Give the extent of all Plasmodium vivax-infected red blood cells.
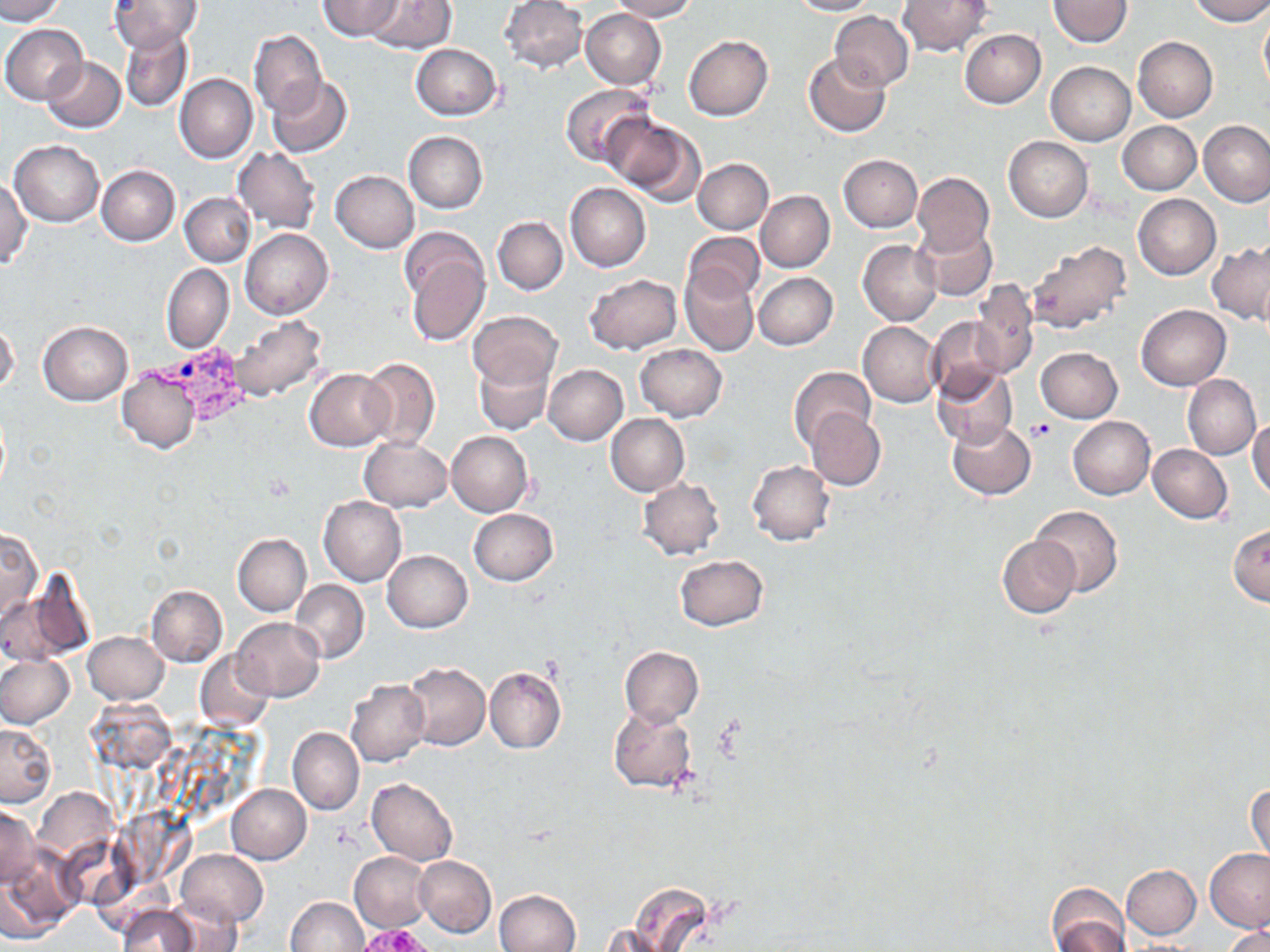

Approximate bounding boxes as named x1/y1/x2/y2 corners in pixels.
Plasmodium vivax-infected red blood cells: (x1=140, y1=342, x2=257, y2=429).

Uninfected red blood cell locations: (x1=0, y1=0, x2=64, y2=24), (x1=318, y1=0, x2=402, y2=40), (x1=363, y1=0, x2=454, y2=53), (x1=500, y1=0, x2=587, y2=73), (x1=610, y1=0, x2=696, y2=21), (x1=787, y1=0, x2=877, y2=17), (x1=899, y1=0, x2=993, y2=57), (x1=1048, y1=0, x2=1133, y2=48), (x1=1188, y1=0, x2=1270, y2=25), (x1=107, y1=1, x2=203, y2=53), (x1=1258, y1=7, x2=1270, y2=96), (x1=580, y1=8, x2=666, y2=90), (x1=830, y1=11, x2=913, y2=90), (x1=1, y1=24, x2=87, y2=105), (x1=120, y1=26, x2=194, y2=112), (x1=248, y1=29, x2=327, y2=118), (x1=960, y1=29, x2=1046, y2=107), (x1=684, y1=34, x2=773, y2=120), (x1=1133, y1=37, x2=1218, y2=121), (x1=411, y1=44, x2=502, y2=121), (x1=803, y1=52, x2=890, y2=137), (x1=42, y1=57, x2=126, y2=132), (x1=1046, y1=61, x2=1135, y2=145), (x1=174, y1=74, x2=257, y2=163), (x1=268, y1=76, x2=353, y2=158), (x1=559, y1=83, x2=653, y2=170), (x1=603, y1=113, x2=703, y2=204), (x1=1198, y1=120, x2=1270, y2=208), (x1=1119, y1=121, x2=1200, y2=194), (x1=404, y1=131, x2=487, y2=213), (x1=1004, y1=136, x2=1093, y2=222), (x1=10, y1=140, x2=104, y2=226), (x1=233, y1=147, x2=322, y2=233), (x1=838, y1=154, x2=923, y2=231), (x1=693, y1=159, x2=773, y2=234), (x1=97, y1=164, x2=180, y2=246), (x1=331, y1=170, x2=419, y2=252), (x1=913, y1=172, x2=994, y2=255), (x1=0, y1=176, x2=31, y2=269), (x1=565, y1=182, x2=651, y2=272), (x1=755, y1=190, x2=834, y2=272), (x1=181, y1=193, x2=254, y2=267), (x1=1133, y1=194, x2=1220, y2=279), (x1=493, y1=217, x2=568, y2=295), (x1=913, y1=223, x2=996, y2=301), (x1=241, y1=229, x2=333, y2=319), (x1=399, y1=232, x2=489, y2=346), (x1=683, y1=232, x2=765, y2=304), (x1=859, y1=240, x2=942, y2=325), (x1=1026, y1=241, x2=1132, y2=335), (x1=1207, y1=242, x2=1270, y2=324), (x1=161, y1=264, x2=234, y2=353), (x1=680, y1=267, x2=758, y2=356), (x1=755, y1=273, x2=838, y2=350), (x1=584, y1=274, x2=681, y2=355), (x1=969, y1=281, x2=1038, y2=379), (x1=1136, y1=305, x2=1231, y2=389), (x1=469, y1=311, x2=561, y2=389), (x1=927, y1=315, x2=1006, y2=400), (x1=228, y1=316, x2=329, y2=401), (x1=37, y1=321, x2=132, y2=405), (x1=858, y1=321, x2=941, y2=407), (x1=0, y1=322, x2=20, y2=395), (x1=635, y1=342, x2=727, y2=421), (x1=1036, y1=347, x2=1123, y2=423), (x1=473, y1=354, x2=553, y2=436), (x1=359, y1=357, x2=440, y2=451), (x1=542, y1=365, x2=628, y2=445), (x1=932, y1=365, x2=1018, y2=448), (x1=117, y1=366, x2=201, y2=453), (x1=305, y1=368, x2=394, y2=451), (x1=789, y1=368, x2=875, y2=452), (x1=1182, y1=374, x2=1260, y2=460), (x1=806, y1=409, x2=886, y2=491), (x1=606, y1=414, x2=689, y2=495), (x1=1068, y1=415, x2=1154, y2=499), (x1=1248, y1=417, x2=1270, y2=500), (x1=946, y1=418, x2=1035, y2=499), (x1=447, y1=430, x2=532, y2=516), (x1=359, y1=436, x2=451, y2=513), (x1=1147, y1=444, x2=1232, y2=523), (x1=747, y1=461, x2=834, y2=546), (x1=638, y1=478, x2=725, y2=560), (x1=319, y1=496, x2=406, y2=588), (x1=1031, y1=505, x2=1123, y2=596), (x1=468, y1=508, x2=558, y2=586), (x1=1228, y1=525, x2=1270, y2=606), (x1=0, y1=526, x2=40, y2=622), (x1=233, y1=533, x2=311, y2=615), (x1=996, y1=535, x2=1080, y2=618), (x1=383, y1=550, x2=473, y2=632), (x1=675, y1=554, x2=768, y2=631), (x1=7, y1=579, x2=92, y2=664), (x1=290, y1=580, x2=369, y2=664), (x1=146, y1=584, x2=227, y2=668), (x1=232, y1=617, x2=325, y2=701), (x1=83, y1=631, x2=169, y2=704), (x1=619, y1=646, x2=704, y2=727), (x1=194, y1=650, x2=275, y2=730), (x1=0, y1=656, x2=74, y2=727), (x1=403, y1=661, x2=491, y2=750), (x1=485, y1=666, x2=567, y2=754), (x1=345, y1=679, x2=430, y2=767), (x1=608, y1=704, x2=699, y2=793), (x1=0, y1=723, x2=56, y2=807), (x1=288, y1=727, x2=364, y2=815), (x1=366, y1=779, x2=457, y2=866), (x1=1247, y1=781, x2=1269, y2=863), (x1=226, y1=784, x2=311, y2=864), (x1=0, y1=804, x2=38, y2=887), (x1=1206, y1=848, x2=1270, y2=933), (x1=176, y1=850, x2=268, y2=928), (x1=349, y1=851, x2=433, y2=933), (x1=0, y1=854, x2=77, y2=943), (x1=413, y1=855, x2=496, y2=937), (x1=1121, y1=864, x2=1201, y2=939), (x1=1046, y1=883, x2=1129, y2=950), (x1=494, y1=889, x2=581, y2=951), (x1=159, y1=897, x2=243, y2=951), (x1=285, y1=897, x2=368, y2=951), (x1=116, y1=904, x2=203, y2=952), (x1=1222, y1=925, x2=1270, y2=952). Platelet locations: (x1=1027, y1=419, x2=1057, y2=440). Slide-level diagnosis: Plasmodium vivax. Single field of view. Light microscopy. Captured at 1000x magnification. May-Grünwald-Giemsa-stained preparation. Image is 1270×952 pixels. Thin blood smear.